Describe the morphology of the red blood cells.
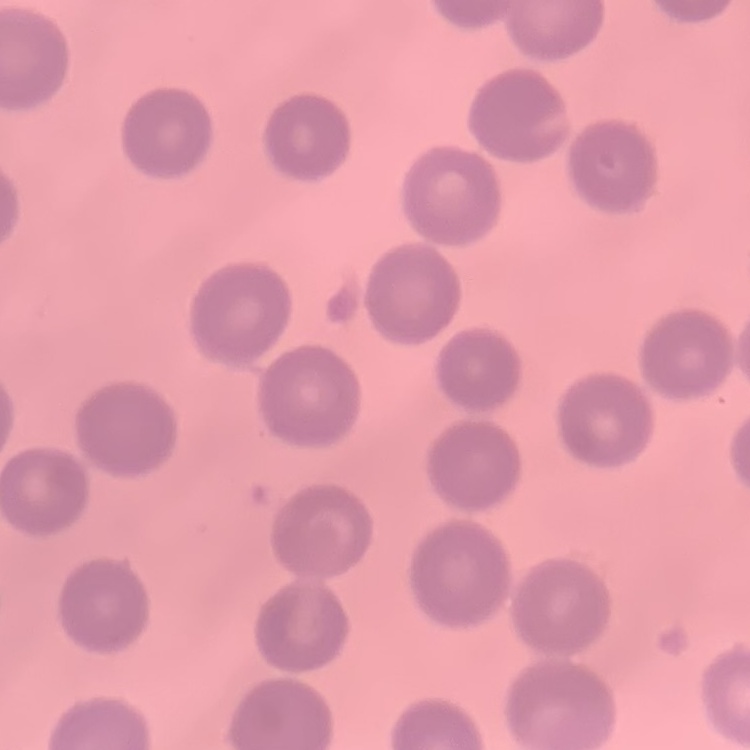

They show no rouleaux formation.

Thin blood smear. Stained with either Field's or Giemsa. Square crop of a larger photomicrograph.